Describe the morphology of the erythrocytes.
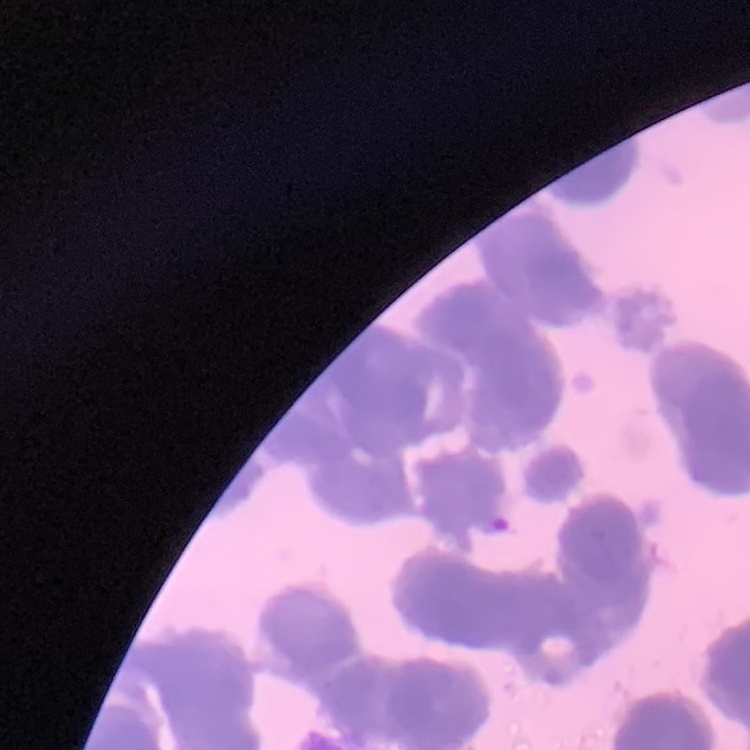
They show rouleaux formation.

{
  "image_type": "one tile cut from a larger photomicrograph",
  "preparation": "thin blood film",
  "stain": "Field's or Giemsa"
}